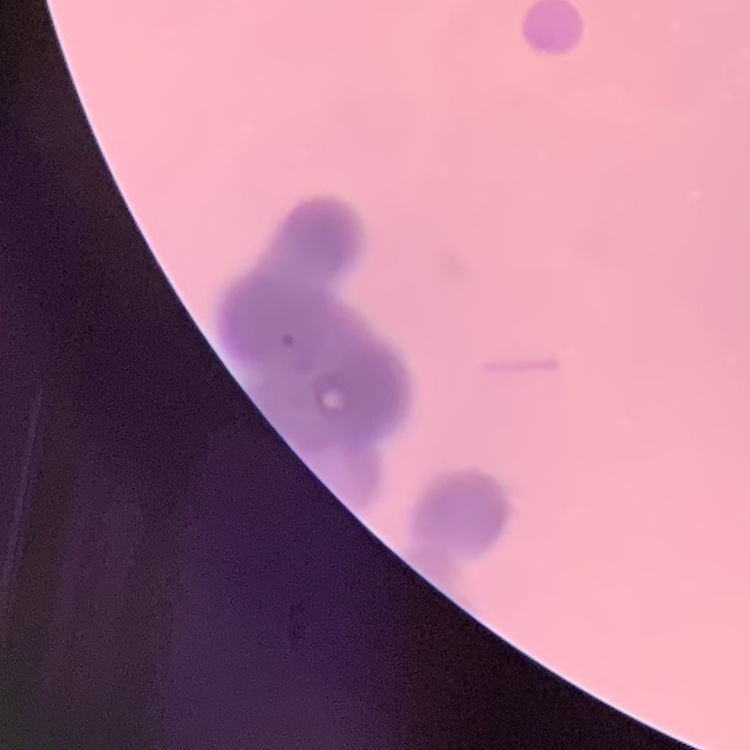 The erythrocytes exhibit rouleaux formation. Stained with either Field's or Giemsa. Thin blood smear. One tile cut from a larger photomicrograph.